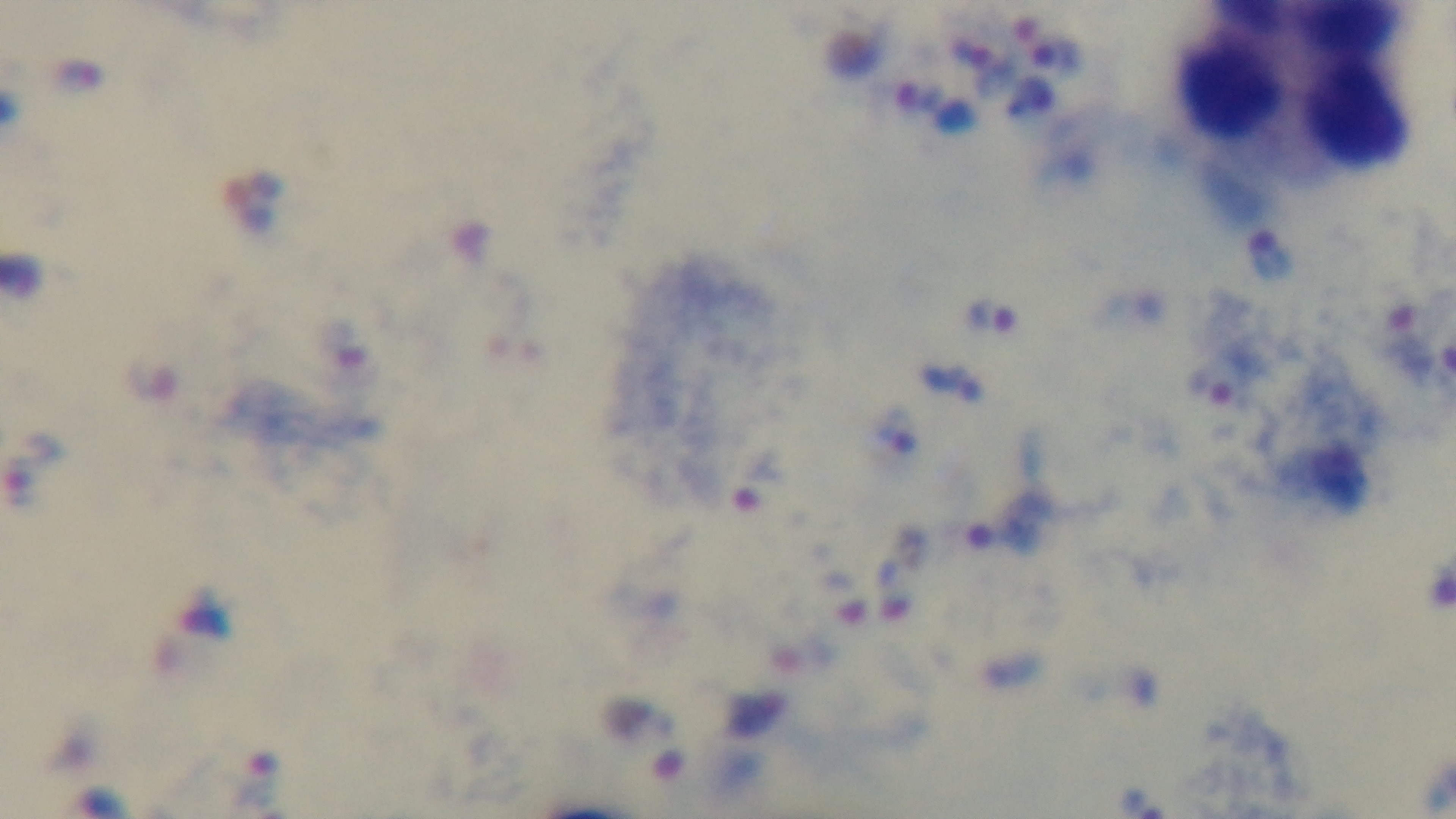

Summary:
  - Malaria status: infected
  - Objective: 100x oil immersion
  - Modality: light microscopy
  - Capture: mounted 4K digital camera
  - Preparation: thick
  - Field of view: single
  - Stain: Giemsa